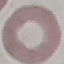
Summary:
  - Result: no malaria parasites seen
  - Image type: cell patch, automatically extracted from a larger field of view and resized to 64 × 64 pixels
  - Stain: Giemsa
  - Preparation: thin blood smear
  - Capture: smartphone camera at the microscope eyepiece